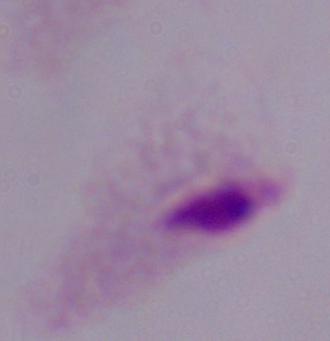
A trichomonad is shown. Micrograph. 1000x magnification.